Classify this cell by malaria status.
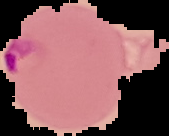
It is parasitized.

{
  "preparation": "thin blood smear",
  "image_size": "169×136 pixels",
  "image_type": "cell region segmented out of the field of view; surrounding area masked to black"
}